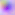

modality = micrograph
magnification = 400x
identification = Toxoplasma gondii